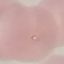 Malaria status: parasitized. Photographed with a smartphone camera at the microscope eyepiece. Giemsa stain. Cell patch, automatically extracted from a larger field of view and resized to 64 × 64 pixels. Thin blood smear.